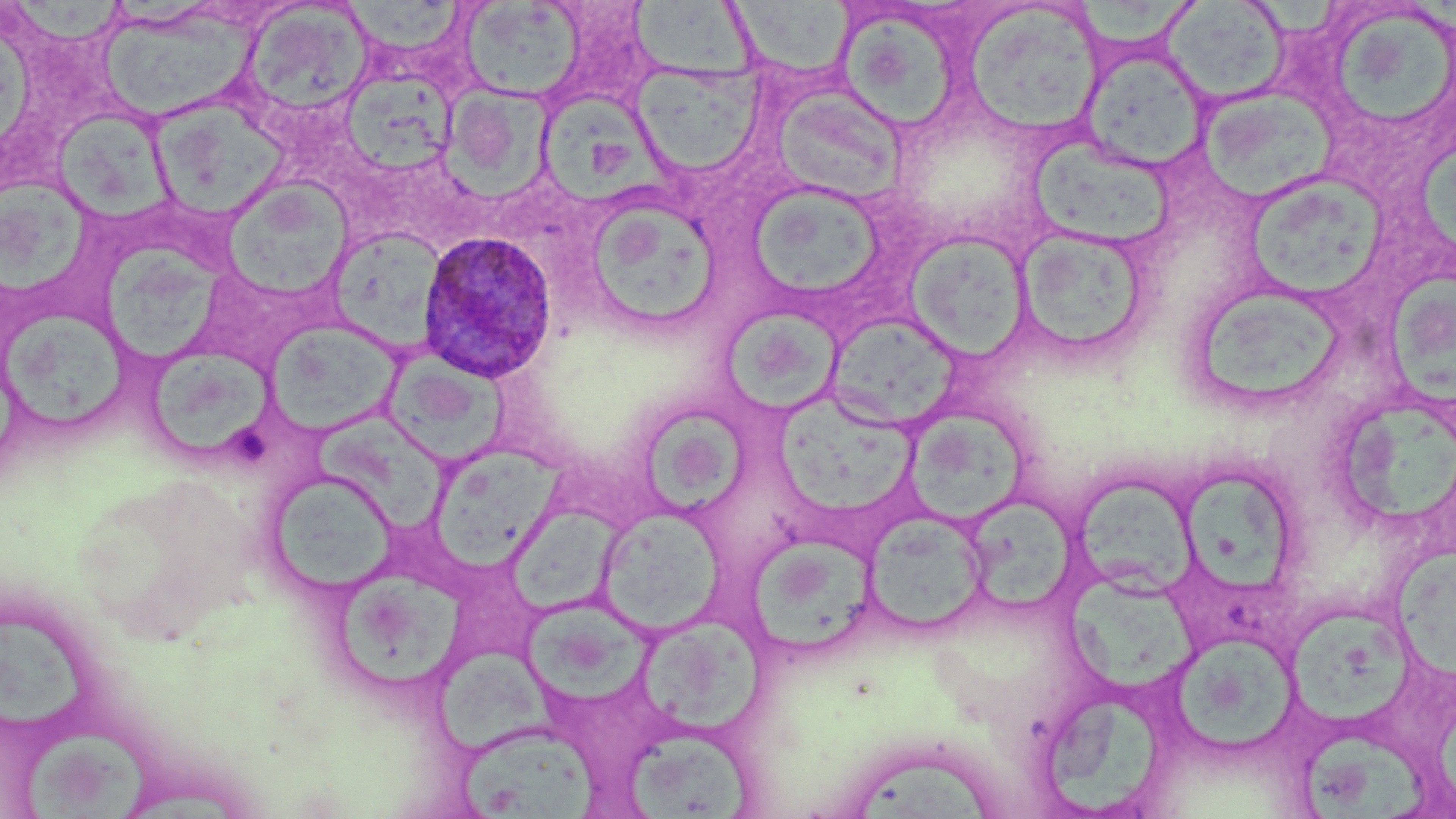
slide-level diagnosis = Plasmodium ovale
preparation = thin blood film
magnification = 1000x
modality = light microscopy
image size = 1456×819 pixels
platelet locations = approximate bounding boxes as [x1, y1, x2, y2] in pixels: [239, 430, 276, 470]
Plasmodium ovale-infected red blood cell locations = approximate bounding boxes as [x1, y1, x2, y2] in pixels: [416, 230, 559, 384]
field of view = one of a larger specimen
stain = May-Grünwald-Giemsa
uninfected red blood cell locations = approximate bounding boxes as [x1, y1, x2, y2] in pixels: [9, 0, 130, 44], [625, 0, 763, 80], [1081, 0, 1203, 53], [1163, 1, 1289, 104], [343, 2, 468, 57], [458, 2, 585, 102], [725, 2, 857, 80], [243, 3, 373, 119], [963, 3, 1105, 137], [1333, 11, 1452, 121], [105, 17, 267, 121], [842, 17, 956, 132], [1079, 46, 1211, 173], [630, 63, 764, 178], [347, 73, 460, 180], [437, 81, 563, 204], [770, 83, 907, 204], [1197, 87, 1335, 205], [155, 94, 291, 216], [536, 94, 678, 204], [50, 112, 178, 222], [1026, 137, 1177, 250], [1414, 139, 1456, 258], [0, 172, 98, 305], [1251, 172, 1392, 300], [222, 178, 353, 299], [745, 182, 889, 304], [581, 192, 723, 333], [330, 227, 447, 352], [1015, 227, 1153, 362], [905, 232, 1032, 360], [99, 241, 231, 367], [1386, 273, 1456, 412], [1196, 290, 1361, 400], [4, 305, 138, 434], [723, 309, 847, 416], [265, 319, 401, 436], [827, 320, 959, 434], [385, 349, 511, 464], [151, 354, 279, 458], [778, 392, 917, 521], [1341, 399, 1456, 519], [645, 403, 755, 519], [908, 407, 1031, 526], [308, 410, 457, 537], [429, 445, 562, 571], [1177, 460, 1294, 608], [265, 468, 397, 597], [1072, 474, 1196, 604], [973, 497, 1081, 615], [500, 503, 633, 616], [596, 508, 725, 635], [863, 511, 991, 638], [751, 529, 882, 655], [1393, 548, 1456, 688], [1064, 562, 1204, 696], [336, 572, 473, 687], [519, 601, 662, 704], [7, 609, 86, 735], [634, 611, 770, 735], [1292, 612, 1418, 727], [1173, 632, 1308, 754], [438, 647, 570, 757], [1042, 695, 1173, 819], [458, 726, 599, 819], [622, 727, 756, 817], [23, 729, 157, 818], [1299, 733, 1428, 819], [849, 753, 993, 819]